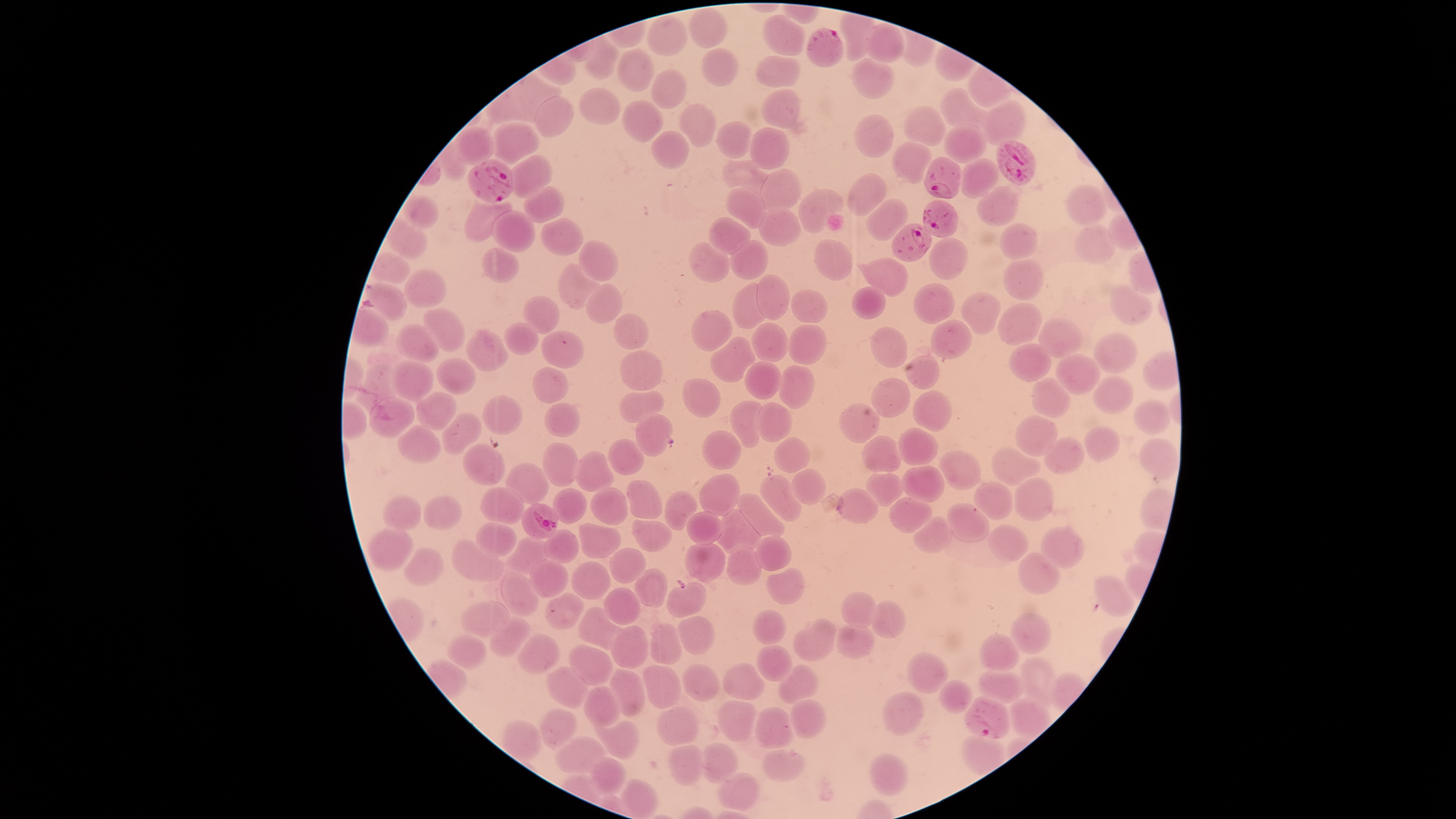 Approximate bounding boxes as {left, top, right, bottom} in pixels. Parasitized RBCs: {806, 28, 844, 68}, {996, 141, 1036, 185}, {925, 157, 961, 199}, {467, 159, 513, 203}, {923, 200, 959, 237}, {892, 223, 931, 262}, {521, 504, 558, 539}, {964, 697, 1009, 740}. Uninfected RBCs: {691, 8, 727, 49}, {648, 14, 687, 56}, {764, 15, 804, 56}, {864, 23, 905, 63}, {584, 34, 618, 79}, {618, 49, 654, 91}, {702, 49, 738, 87}, {757, 56, 801, 87}, {851, 58, 894, 100}, {651, 69, 687, 109}, {579, 87, 620, 127}, {940, 87, 988, 128}, {761, 89, 801, 128}, {534, 96, 574, 138}, {622, 100, 663, 142}, {980, 100, 1026, 147}, {679, 105, 716, 147}, {904, 106, 947, 147}, {855, 114, 893, 158}, {716, 120, 751, 159}, {493, 122, 539, 165}, {942, 124, 989, 163}, {455, 126, 494, 165}, {749, 127, 789, 169}, {652, 130, 689, 169}, {892, 142, 931, 184}, {508, 155, 552, 197}, {958, 158, 998, 197}, {721, 160, 773, 195}, {761, 169, 801, 212}, {847, 174, 886, 216}, {524, 186, 564, 222}, {727, 186, 767, 229}, {976, 186, 1018, 227}, {1066, 186, 1106, 226}, {798, 189, 844, 233}, {401, 195, 439, 228}, {866, 198, 909, 242}, {464, 200, 512, 243}, {758, 209, 798, 247}, {492, 211, 535, 253}, {386, 218, 428, 259}, {541, 218, 583, 255}, {707, 218, 750, 254}, {999, 223, 1039, 261}, {1074, 225, 1116, 264}, {929, 238, 968, 280}, {578, 240, 619, 283}, {730, 240, 769, 280}, {814, 240, 853, 280}, {689, 242, 730, 283}, {480, 248, 521, 284}, {371, 253, 410, 283}, {856, 258, 909, 296}, {1003, 259, 1043, 302}, {558, 263, 601, 309}, {404, 270, 446, 307}, {757, 275, 789, 319}, {365, 283, 408, 320}, {585, 284, 623, 324}, {733, 284, 767, 329}, {913, 284, 954, 325}, {1109, 285, 1153, 325}, {850, 286, 887, 320}, {790, 290, 827, 323}, {961, 292, 1002, 335}, {523, 296, 559, 335}, {998, 304, 1043, 345}, {423, 307, 465, 352}, {690, 310, 732, 351}, {614, 312, 650, 350}, {1037, 318, 1082, 359}, {932, 320, 974, 359}, {503, 322, 539, 356}, {752, 323, 788, 362}, {396, 324, 439, 363}, {789, 325, 825, 366}, {871, 328, 908, 368}, {466, 329, 508, 372}, {541, 330, 584, 369}, {1093, 333, 1136, 375}, {710, 337, 755, 382}, {1009, 343, 1050, 382}, {620, 351, 662, 390}, {1056, 354, 1101, 395}, {906, 355, 939, 390}, {436, 358, 475, 396}, {355, 359, 404, 416}, {390, 361, 433, 401}, {745, 361, 781, 400}, {779, 365, 814, 409}, {533, 366, 569, 404}, {1092, 376, 1134, 415}, {1031, 377, 1071, 420}, {683, 378, 721, 418}, {872, 378, 910, 418}, {620, 391, 663, 423}, {912, 391, 952, 432}, {416, 392, 456, 430}, {483, 395, 523, 435}, {368, 397, 415, 439}, {1133, 400, 1170, 434}, {729, 401, 763, 448}, {757, 402, 792, 442}, {543, 403, 581, 437}, {839, 403, 880, 444}, {443, 412, 481, 454}, {635, 414, 672, 456}, {1015, 415, 1059, 457}, {397, 425, 441, 463}, {1084, 425, 1119, 462}, {898, 427, 938, 467}, {703, 431, 742, 469}, {862, 436, 900, 472}, {775, 437, 809, 473}, {1043, 438, 1085, 473}, {607, 439, 645, 475}, {1139, 439, 1180, 481}, {542, 443, 578, 486}, {462, 444, 505, 486}, {991, 447, 1040, 485}, {575, 450, 614, 492}, {939, 451, 980, 492}, {506, 463, 549, 505}, {901, 465, 946, 503}, {792, 468, 827, 505}, {866, 473, 903, 507}, {700, 474, 741, 516}, {761, 475, 803, 522}, {1014, 478, 1055, 522}, {627, 481, 663, 520}, {975, 482, 1013, 520}, {480, 487, 525, 524}, {553, 488, 586, 525}, {591, 488, 629, 526}, {836, 490, 879, 524}, {664, 492, 697, 531}, {735, 493, 785, 536}, {382, 495, 420, 530}, {423, 496, 460, 530}, {890, 497, 931, 535}, {947, 503, 989, 542}, {718, 508, 760, 552}, {687, 512, 723, 545}, {913, 517, 951, 554}, {633, 520, 672, 553}, {476, 522, 517, 556}, {580, 523, 619, 558}, {988, 524, 1028, 561}, {1041, 526, 1085, 568}, {367, 527, 413, 572}, {544, 529, 579, 564}, {507, 535, 550, 574}, {755, 535, 792, 571}, {453, 540, 504, 583}, {685, 544, 725, 582}, {727, 546, 763, 584}, {403, 548, 444, 587}, {611, 548, 647, 584}, {1017, 552, 1059, 595}, {530, 560, 567, 598}, {572, 562, 611, 600}, {766, 568, 805, 605}, {635, 569, 668, 608}, {502, 573, 539, 617}, {1093, 576, 1134, 617}, {666, 583, 707, 618}, {604, 587, 641, 625}, {841, 592, 876, 627}, {545, 593, 583, 629}, {462, 602, 510, 638}, {872, 602, 906, 639}, {578, 607, 621, 650}, {753, 610, 786, 645}, {1011, 614, 1052, 655}, {490, 616, 531, 656}, {677, 616, 715, 655}, {795, 617, 836, 662}, {651, 623, 682, 664}, {837, 625, 875, 659}, {611, 626, 647, 668}, {446, 635, 487, 669}, {517, 635, 560, 676}, {979, 636, 1019, 672}, {757, 644, 793, 683}, {568, 646, 614, 686}, {905, 655, 949, 693}, {1019, 658, 1055, 710}, {722, 662, 765, 699}, {683, 664, 718, 701}, {779, 664, 817, 704}, {642, 666, 681, 710}, {548, 667, 588, 707}, {978, 669, 1026, 704}, {611, 670, 645, 717}, {938, 680, 974, 715}, {585, 685, 620, 726}, {882, 692, 923, 736}, {790, 698, 827, 739}, {1009, 699, 1051, 740}, {717, 700, 756, 741}, {656, 706, 700, 745}, {755, 707, 791, 747}, {540, 709, 577, 748}, {502, 720, 541, 762}, {593, 720, 638, 759}, {555, 737, 604, 775}, {702, 743, 737, 784}, {668, 745, 704, 786}, {763, 749, 805, 782}, {869, 753, 909, 797}, {590, 757, 627, 794}, {716, 773, 758, 811}, {621, 779, 658, 819}. One field of view of the specimen. Species: Plasmodium falciparum. Giemsa-stained preparation. Presence: malaria parasites seen. Circular visible region. Smartphone photograph through the microscope eyepiece. Thin smear of blood. Image is 1456×819 pixels.